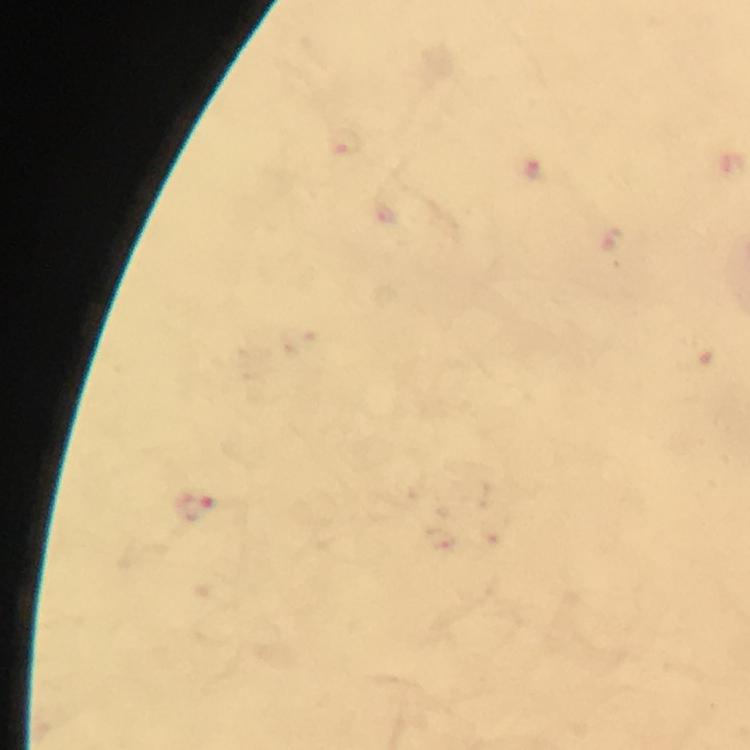

immersion oil = used
context = from a malaria diagnostic workup
cropped from = one field of view
magnification = 100x
capture = smartphone camera through the microscope
image size = 750×750 pixels
preparation = thick smear
stain = Giemsa
Plasmodium parasite locations = approximate centers as {x, y} in pixels: {197, 507}